Report the malaria status of this cell.
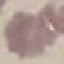

It is uninfected.

Summary:
  - Capture: smartphone through the microscope eyepiece
  - Image type: cell patch, automatically extracted from a larger field of view and resized to 64 × 64 pixels
  - Preparation: thin blood film
  - Stain: Giemsa